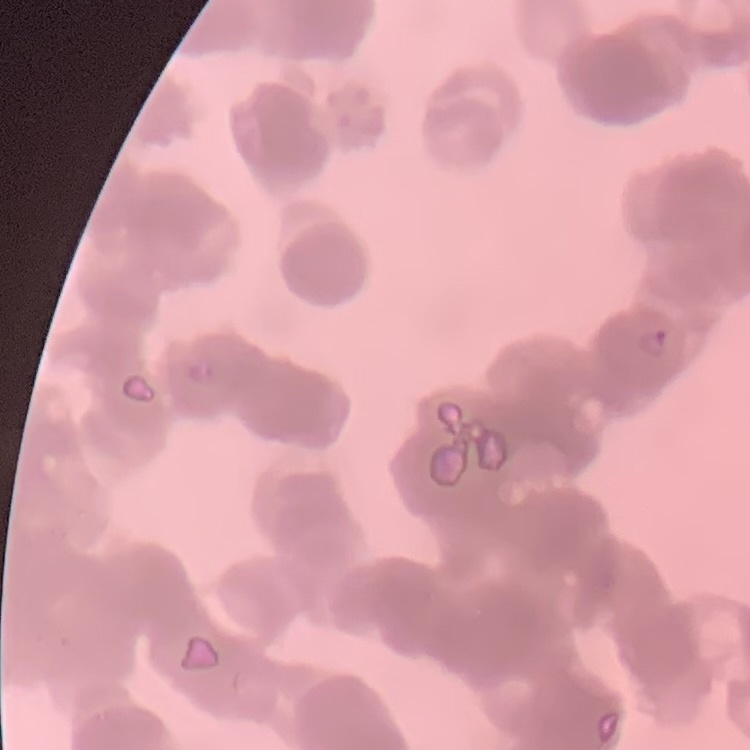

Summary:
  - Erythrocyte morphology: rouleaux formation
  - Image type: square crop of a larger photomicrograph
  - Preparation: thin blood film
  - Stain: Field's or Giemsa